Identify the blood parasite species.
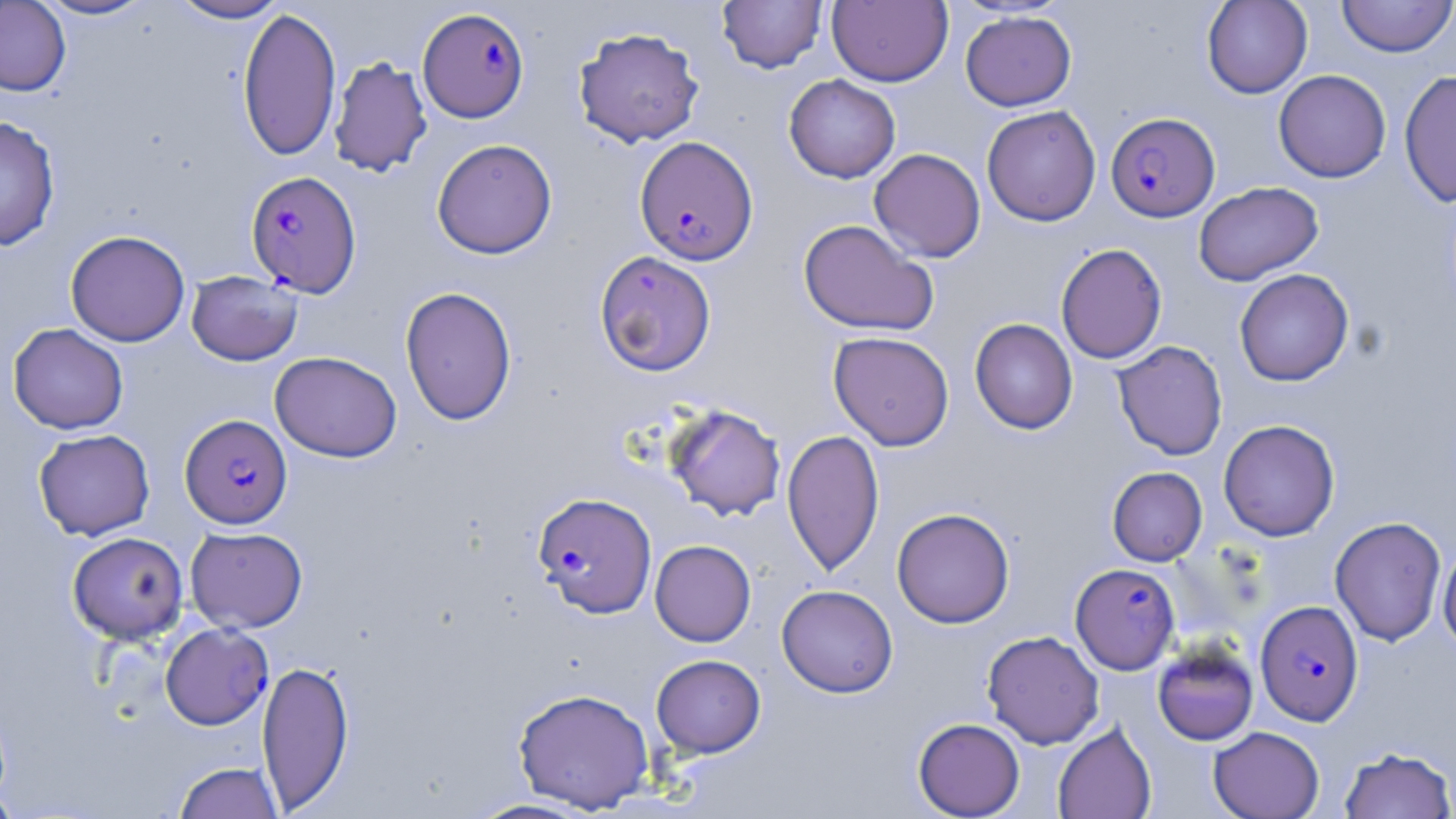
Plasmodium falciparum.

Approximate bounding boxes as (x1, y1, x2, y2) in pixels. Uninfected red blood cell locations: (34, 0, 157, 21), (168, 0, 288, 23), (717, 0, 827, 74), (827, 0, 953, 87), (1202, 0, 1313, 99), (1338, 0, 1456, 58), (0, 1, 71, 96), (237, 6, 342, 162), (960, 11, 1076, 111), (573, 26, 705, 148), (329, 55, 432, 177), (1273, 69, 1391, 182), (1399, 70, 1456, 209), (784, 74, 901, 183), (981, 105, 1101, 226), (0, 115, 61, 251), (431, 138, 557, 259), (869, 148, 986, 263), (1194, 181, 1323, 285), (798, 219, 939, 337), (65, 230, 190, 347), (1056, 243, 1167, 364), (594, 250, 717, 376), (1234, 268, 1354, 386), (186, 271, 303, 366), (400, 286, 517, 426), (969, 318, 1077, 434), (8, 322, 129, 434), (828, 331, 954, 450), (1112, 340, 1228, 460), (269, 351, 402, 462), (663, 404, 786, 521), (1218, 419, 1340, 541), (782, 428, 884, 576), (33, 429, 155, 540), (1107, 467, 1207, 565), (892, 507, 1015, 628), (1330, 516, 1446, 646), (185, 526, 308, 633), (67, 531, 188, 644), (650, 540, 756, 646), (1438, 544, 1456, 652), (776, 584, 898, 698), (982, 630, 1104, 749), (1152, 642, 1258, 746), (651, 654, 766, 757), (257, 659, 355, 812), (512, 687, 656, 813), (913, 717, 1025, 818), (1053, 722, 1157, 819), (1208, 726, 1325, 819), (1339, 746, 1456, 819), (172, 761, 284, 818), (0, 785, 22, 818), (467, 798, 595, 818). Plasmodium falciparum-infected red blood cell locations: (417, 7, 530, 123), (1106, 112, 1220, 221), (634, 136, 758, 265), (245, 170, 362, 297), (180, 414, 292, 528), (533, 492, 657, 618), (1070, 563, 1180, 674), (1255, 600, 1363, 725), (160, 622, 273, 730). Thin blood film. Single field of view. 1000x magnification. Image is 1456×819 pixels. Light microscopy. May-Grünwald-Giemsa stain.